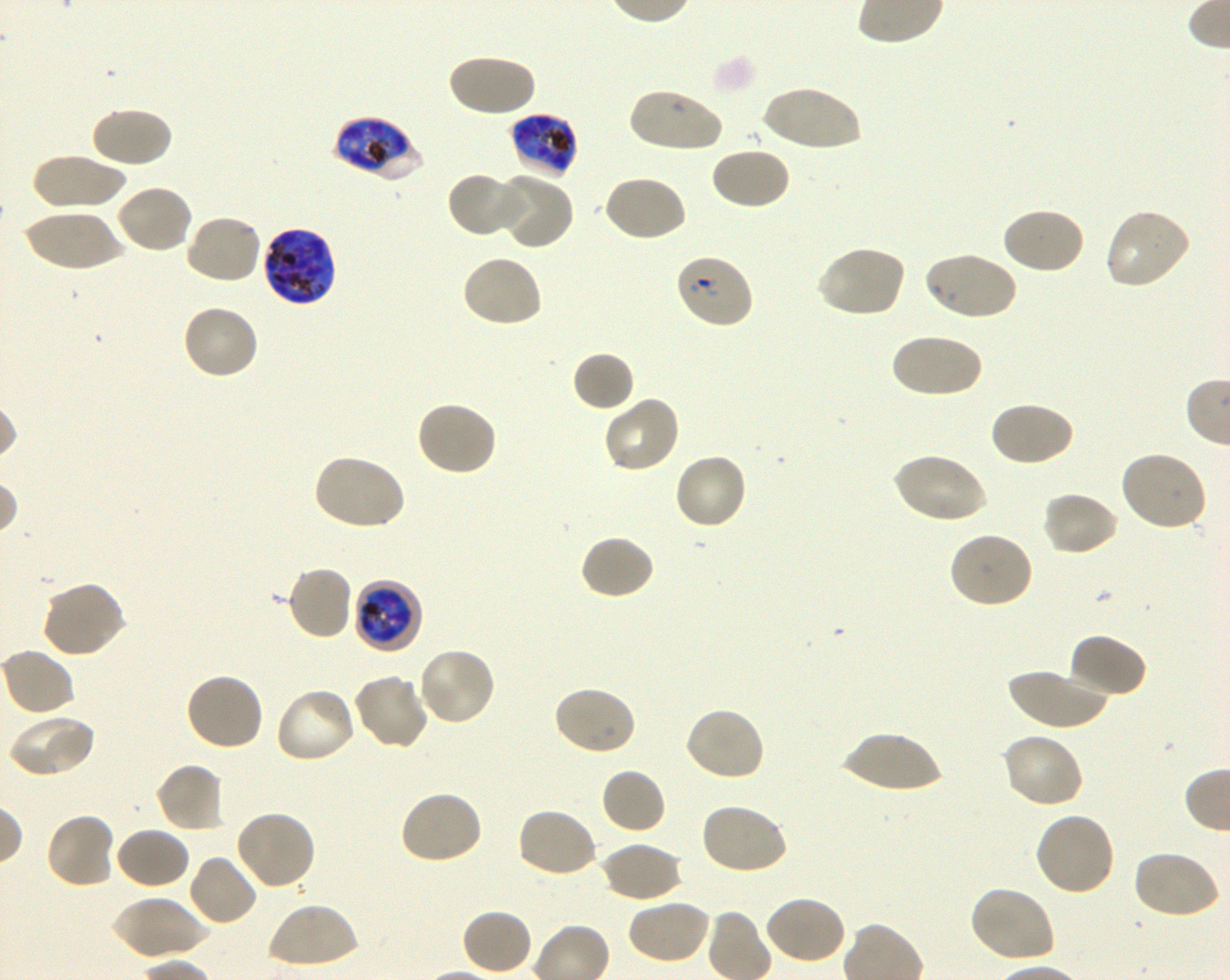

Approximate bounding boxes as [x1, y1, x2, y2] in pixels. Not every red blood cell is marked. A life-cycle stage — or a range of stages, where the recorded stages span more than one — follows each staged infected red blood cell. Locations of red blood cells of indeterminate infection status: [674, 253, 754, 330]. Locations of infected red blood cells: [510, 112, 579, 181] late trophozoite to late schizont; [334, 117, 420, 181] late trophozoite to late schizont; [261, 226, 338, 307] late trophozoite to late schizont; [353, 579, 424, 654] late trophozoite to early schizont. Locations of uninfected red blood cells: [447, 52, 536, 118], [759, 85, 863, 152], [626, 88, 726, 152], [89, 105, 173, 169], [709, 146, 790, 211], [30, 154, 127, 211], [447, 171, 525, 237], [494, 171, 574, 250], [602, 173, 688, 243], [115, 183, 194, 256], [1002, 206, 1086, 275], [1104, 208, 1192, 291], [22, 210, 125, 273], [185, 213, 263, 285], [816, 244, 907, 318], [922, 250, 1017, 322], [461, 253, 544, 329], [181, 303, 261, 381], [889, 332, 983, 399], [572, 351, 636, 413], [602, 395, 682, 475], [414, 400, 497, 477], [990, 400, 1075, 468], [892, 450, 988, 524], [1119, 450, 1208, 532], [673, 452, 750, 531], [311, 453, 407, 531], [1041, 490, 1119, 557], [948, 532, 1035, 609], [579, 534, 656, 601], [285, 564, 354, 641], [39, 580, 126, 659], [1067, 633, 1147, 700], [1, 648, 76, 718], [416, 648, 496, 727], [1005, 666, 1111, 730], [185, 671, 265, 752], [352, 672, 429, 750], [552, 685, 637, 756], [274, 687, 358, 765], [683, 706, 767, 782], [7, 714, 95, 779], [842, 731, 944, 794], [1000, 731, 1085, 808], [155, 762, 225, 833], [599, 767, 666, 835], [399, 790, 484, 866], [699, 802, 789, 876], [516, 807, 598, 879], [235, 808, 317, 890], [44, 811, 117, 889], [1032, 811, 1115, 898], [115, 827, 191, 891], [600, 841, 682, 904], [1131, 850, 1221, 921], [186, 853, 258, 927], [969, 885, 1056, 965], [762, 895, 848, 965], [110, 896, 209, 961], [626, 899, 711, 964], [266, 901, 358, 969], [461, 908, 533, 976]. Image is 1230×980 pixels. Blood group of the donor: O+. Plasmodium falciparum strain 3D7 maintained in shaking in-vitro culture. Single field of view. 100x objective under oil immersion, numerical aperture 1.30. Giemsa stain. Thin blood smear.